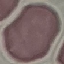

Summary:
  - Result: no malaria parasites detected
  - Image type: cell patch, automatically extracted from a larger field of view and resized to 64 × 64 pixels
  - Preparation: thin blood smear
  - Stain: Giemsa
  - Capture: smartphone camera at the microscope eyepiece